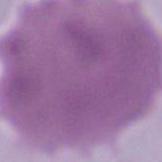

Micrograph. A red blood cell is seen. Captured at 1000x magnification.